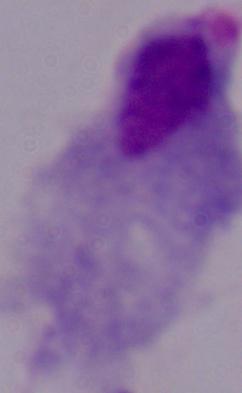 Captured at 1000x magnification. Photomicrograph. A trichomonad is seen.